Classify this cell by malaria status.
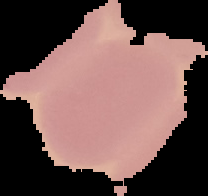
It is uninfected.

image type = segmented cell region with the area outside set to black
image size = 208×196 pixels
preparation = thin blood smear